Find each WBC.
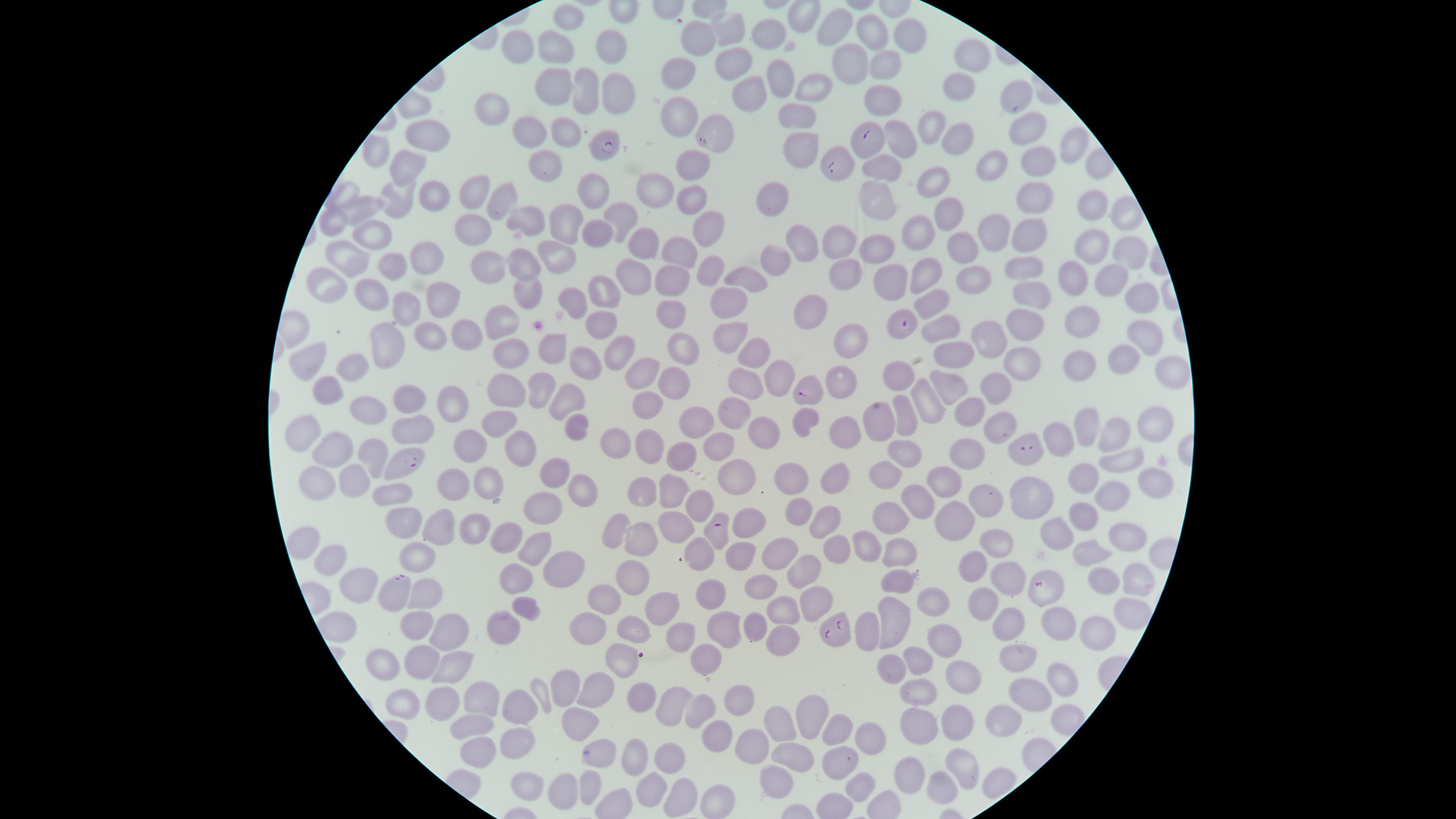
No WBCs identified.

{
  "preparation": "thin blood film",
  "parasitized_RBCs": "approximate marker points as (x, y) in pixels: (714, 130), (869, 141), (607, 145), (835, 166), (903, 324), (809, 391), (1029, 452), (402, 460), (718, 534), (1043, 589), (395, 590), (833, 629)",
  "image_size": "1456×819 pixels",
  "capture": "smartphone photograph through the microscope eyepiece",
  "visible_region": "circular",
  "species": "Plasmodium falciparum",
  "presence": "malaria parasites identified",
  "uninfected_RBCs": "approximate marker points as (x, y) in pixels: (567, 21), (837, 27), (728, 30), (869, 33), (902, 36), (773, 38), (701, 39), (613, 49), (512, 50), (554, 50), (971, 55), (850, 61), (732, 63), (887, 67), (779, 75), (682, 77), (555, 83), (808, 86), (963, 87), (587, 92), (612, 93), (747, 94), (1013, 96), (884, 103), (494, 108), (675, 117), (796, 117), (1024, 126), (929, 129), (565, 131), (535, 134), (428, 136), (904, 140), (955, 142), (1066, 145), (375, 149), (799, 151), (691, 163), (987, 163), (410, 164), (547, 164), (883, 167), (1037, 169), (936, 178), (594, 188), (655, 190), (343, 194), (431, 194), (471, 195), (776, 196), (876, 196), (496, 198), (1029, 198), (395, 200), (689, 200), (1090, 203), (368, 209), (950, 214), (618, 216), (529, 220), (704, 220), (567, 222), (330, 225), (922, 225), (473, 229), (995, 231), (599, 232), (801, 235), (374, 237), (1028, 237), (639, 239), (840, 239), (1088, 245), (879, 248), (966, 248), (674, 249), (1128, 250), (352, 253), (559, 253), (430, 254), (779, 255), (708, 262), (392, 264), (485, 265), (527, 265), (1019, 265), (842, 267), (633, 272), (754, 274), (924, 274), (968, 276), (1072, 279), (1112, 280), (323, 282), (885, 282), (673, 284), (530, 291), (1030, 292), (368, 293), (1140, 293), (597, 295), (574, 297), (435, 298), (934, 301), (407, 305), (730, 308), (668, 313), (812, 314), (501, 318), (601, 321), (1077, 322), (1019, 324), (459, 326), (938, 330), (427, 333), (730, 336), (1142, 336), (389, 338), (989, 339), (852, 341), (678, 344), (548, 347), (505, 349), (754, 353), (956, 355), (307, 356), (1123, 356), (614, 358), (585, 359), (1016, 367), (1075, 368), (349, 370), (1169, 371), (642, 373), (776, 375), (901, 376), (746, 377), (842, 380), (675, 383), (543, 384), (993, 384), (951, 386), (322, 393), (501, 393), (409, 397), (926, 401), (564, 402), (444, 403), (649, 403), (368, 408), (968, 410), (732, 412), (904, 415), (878, 419), (806, 420), (702, 422), (1091, 424), (306, 427), (499, 427), (1151, 427), (411, 429), (571, 429), (995, 429), (847, 433), (1119, 433), (1066, 435), (771, 437), (618, 442), (651, 444), (715, 445), (522, 448), (961, 450), (332, 451), (475, 451), (906, 456), (376, 457), (682, 457), (1116, 463), (732, 469), (891, 474), (555, 475), (792, 475), (940, 475), (1086, 476), (1145, 478), (354, 481), (834, 481), (489, 482), (639, 483), (668, 484), (457, 487), (314, 490), (579, 491), (1111, 494), (1025, 495), (919, 496), (989, 497), (383, 498), (689, 501), (545, 506), (1082, 511), (888, 514), (800, 516), (960, 516), (751, 521), (821, 521), (404, 523), (673, 523), (475, 524), (615, 529), (1057, 530), (437, 533), (510, 535), (1122, 538), (301, 540), (633, 540), (871, 541), (536, 543), (832, 545), (995, 545), (693, 552), (1089, 552), (420, 553), (788, 553), (894, 554), (732, 557), (328, 561), (558, 565), (973, 567), (805, 573), (634, 577), (356, 579), (521, 580), (894, 581), (1133, 581), (1009, 582), (1101, 583), (769, 585), (426, 590), (601, 595), (710, 598), (660, 601), (810, 602), (934, 602), (989, 602), (783, 611), (1127, 612), (523, 613), (890, 619), (1065, 621), (756, 623), (412, 625), (503, 625), (1007, 625), (1096, 625), (591, 626), (720, 628), (631, 630), (868, 631), (451, 632), (781, 633), (947, 636), (684, 638), (626, 656), (918, 656), (380, 661), (424, 661), (704, 661), (1019, 662), (894, 667), (452, 672), (1059, 673), (961, 675), (568, 690), (593, 690), (921, 691), (1032, 692), (540, 693), (643, 696), (481, 698), (744, 699), (406, 701), (672, 702), (439, 704), (509, 708), (702, 708), (810, 716), (1006, 719), (578, 723), (959, 725), (779, 726), (917, 726), (838, 730), (474, 731), (717, 737), (759, 738), (861, 742), (514, 745), (635, 754), (598, 755), (787, 755), (474, 756), (672, 759), (963, 762), (838, 766), (911, 774), (944, 780), (526, 781), (654, 781), (774, 783), (866, 784), (590, 787), (679, 796), (559, 798), (714, 798)",
  "field_of_view": "single",
  "stain": "Giemsa"
}